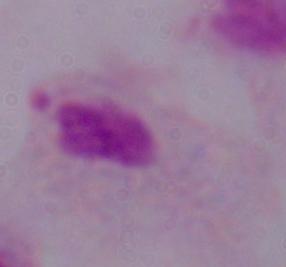
Summary:
  - Modality: photomicrograph
  - Magnification: 1000x
  - Identification: trichomonad